Point out every malaria parasite and every leukocyte.
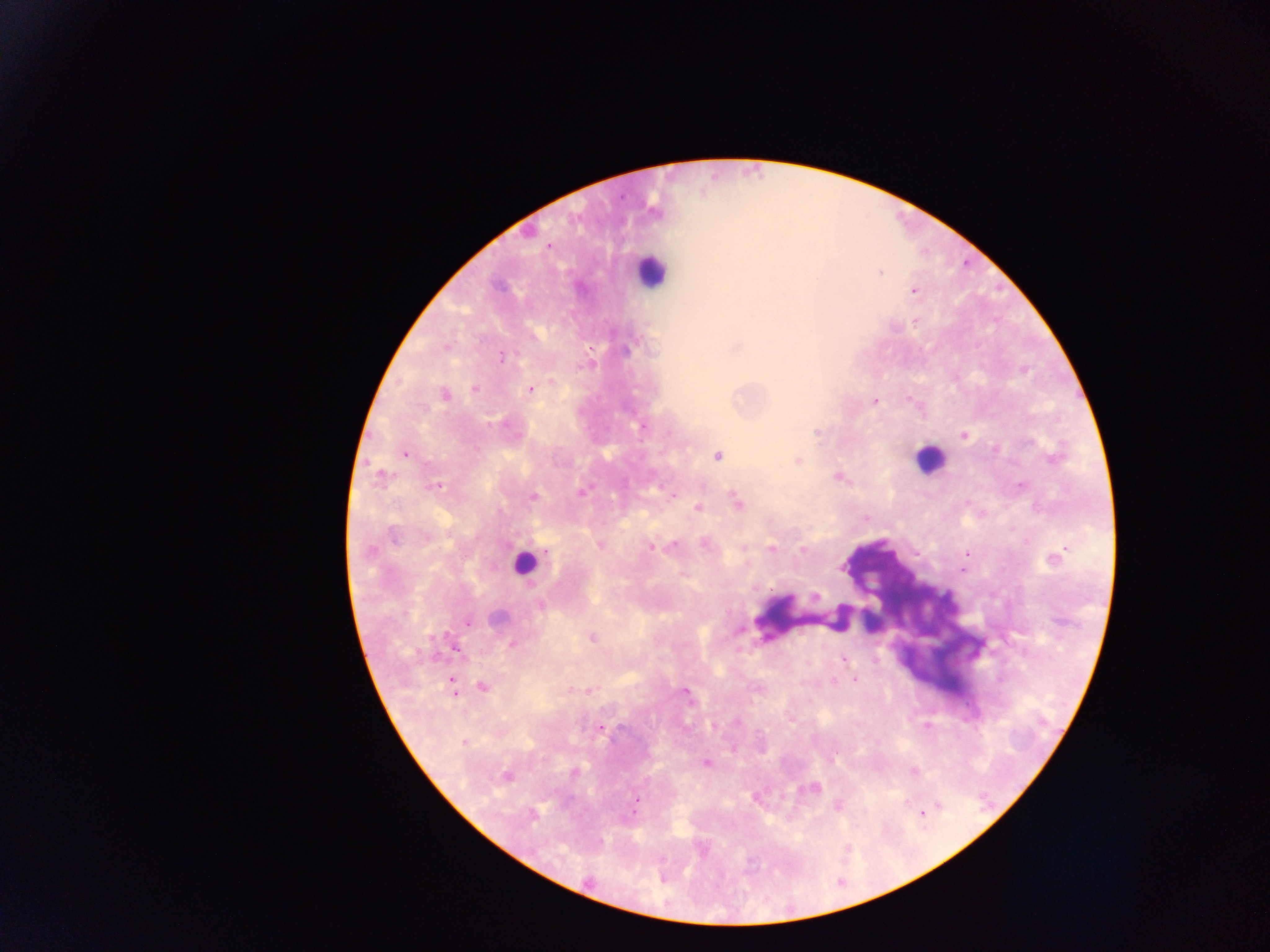

Approximate centers as x y in pixels.
Malaria parasites: 548 245; 880 272; 913 291; 627 350; 501 357; 551 382; 474 389; 530 390; 445 394; 910 398; 875 402; 643 427; 817 432; 964 436; 405 453; 717 455; 797 460; 379 475; 838 477; 437 485; 1021 486; 581 492; 533 497; 737 501; 698 507; 394 536; 704 543; 601 545; 651 546; 673 546; 743 547; 771 547; 803 549; 369 551; 1055 558; 814 596; 497 617; 467 623; 592 638; 512 643; 843 659; 855 679; 452 686; 482 687; 587 691; 685 692; 736 722; 600 728; 464 742; 832 760; 706 763; 914 771; 575 772; 506 776; 813 787; 636 801; 838 805; 939 805; 634 809; 533 815; 923 815.
Leukocytes: 650 271; 929 458; 523 562.

image_size: 1270×952 pixels
preparation: thick blood smear
capture: mobile-phone photograph through a microscope
field_of_view: single
country: Ghana